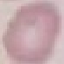

malaria status = uninfected
stain = Giemsa
capture = smartphone camera at the microscope eyepiece
image type = automatically extracted cell patch, resized to 64 × 64 pixels
preparation = thin smear